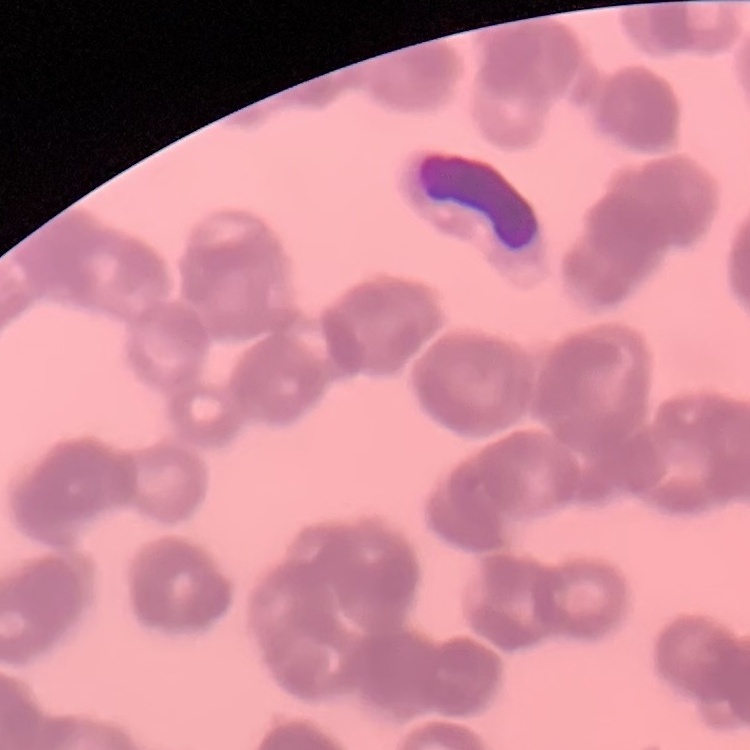

Summary:
  - Erythrocyte morphology: rouleaux formation
  - Preparation: thin peripheral smear
  - Image type: square crop of a larger photomicrograph
  - Stain: Field's or Giemsa